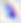
magnification = 400x
modality = photomicrograph
identification = Toxoplasma gondii